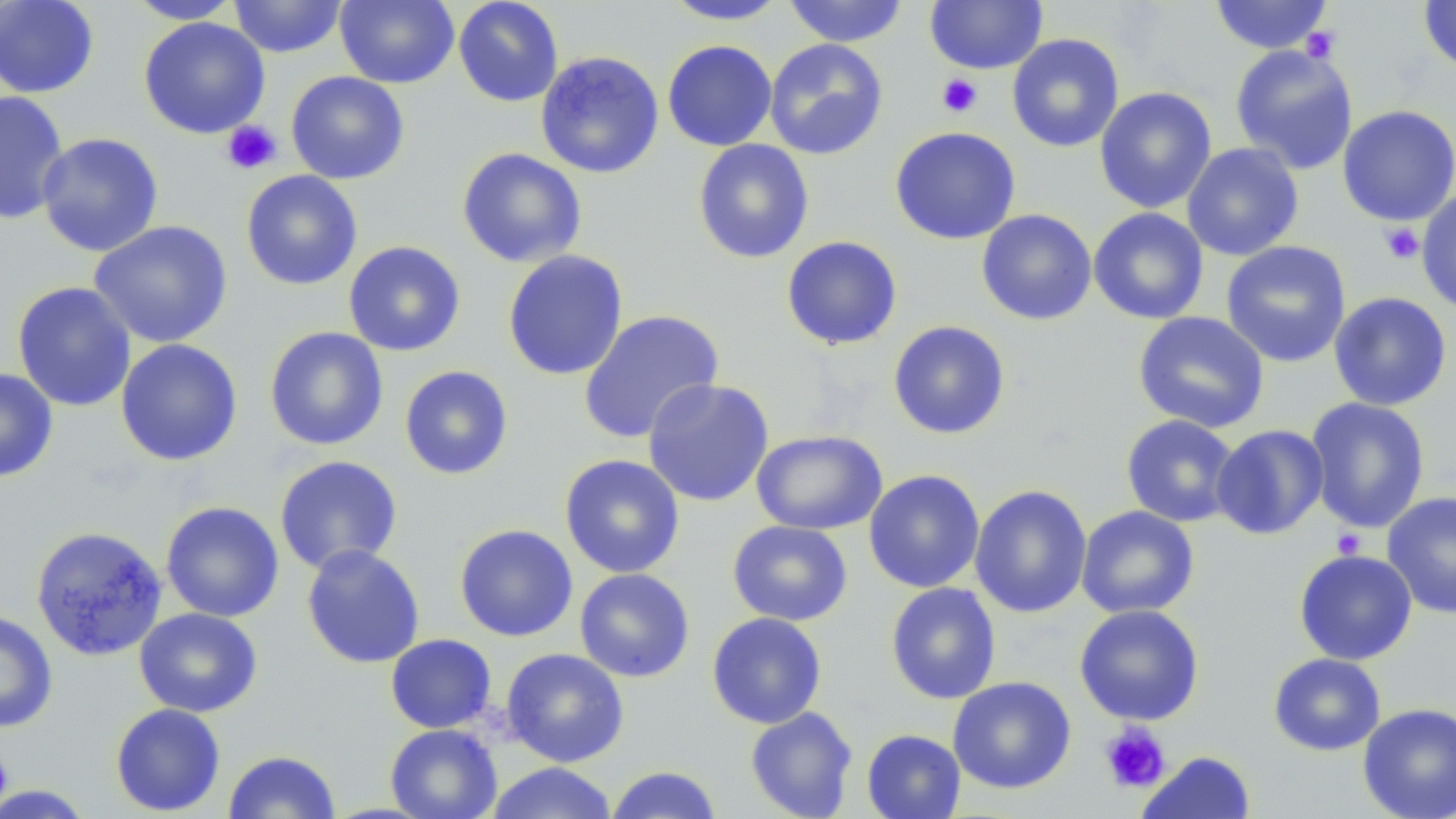
Summary:
  - Coordinate format: approximate bounding boxes as named x1/y1/x2/y2 corners in pixels
  - Platelet locations: (x1=1300, y1=26, x2=1341, y2=63), (x1=937, y1=73, x2=982, y2=118), (x1=221, y1=120, x2=283, y2=175), (x1=1379, y1=222, x2=1425, y2=265), (x1=1331, y1=528, x2=1366, y2=558), (x1=1099, y1=723, x2=1171, y2=793), (x1=0, y1=750, x2=13, y2=806)
  - Uninfected red blood cell locations: (x1=0, y1=0, x2=100, y2=98), (x1=126, y1=0, x2=244, y2=24), (x1=228, y1=0, x2=347, y2=58), (x1=335, y1=0, x2=459, y2=88), (x1=453, y1=0, x2=564, y2=107), (x1=783, y1=0, x2=910, y2=47), (x1=924, y1=0, x2=1048, y2=74), (x1=1209, y1=0, x2=1334, y2=55), (x1=662, y1=1, x2=790, y2=25), (x1=1418, y1=1, x2=1456, y2=74), (x1=138, y1=16, x2=270, y2=139), (x1=1007, y1=33, x2=1124, y2=152), (x1=764, y1=38, x2=888, y2=160), (x1=662, y1=40, x2=777, y2=152), (x1=1230, y1=44, x2=1358, y2=174), (x1=535, y1=51, x2=664, y2=179), (x1=286, y1=71, x2=410, y2=185), (x1=1095, y1=86, x2=1217, y2=214), (x1=1, y1=90, x2=70, y2=226), (x1=1337, y1=105, x2=1456, y2=226), (x1=889, y1=126, x2=1020, y2=245), (x1=37, y1=132, x2=164, y2=257), (x1=692, y1=139, x2=814, y2=264), (x1=1182, y1=142, x2=1304, y2=261), (x1=456, y1=148, x2=587, y2=268), (x1=240, y1=170, x2=363, y2=290), (x1=1416, y1=189, x2=1456, y2=315), (x1=1089, y1=207, x2=1209, y2=324), (x1=976, y1=209, x2=1097, y2=325), (x1=89, y1=220, x2=232, y2=348), (x1=780, y1=235, x2=903, y2=350), (x1=1221, y1=240, x2=1351, y2=367), (x1=343, y1=241, x2=465, y2=357), (x1=502, y1=250, x2=629, y2=381), (x1=12, y1=281, x2=137, y2=412), (x1=1329, y1=291, x2=1452, y2=411), (x1=578, y1=310, x2=724, y2=445), (x1=1133, y1=312, x2=1269, y2=433), (x1=887, y1=320, x2=1011, y2=440), (x1=264, y1=327, x2=388, y2=451), (x1=115, y1=339, x2=243, y2=466), (x1=399, y1=365, x2=513, y2=480), (x1=0, y1=368, x2=58, y2=482), (x1=642, y1=378, x2=774, y2=507), (x1=1305, y1=397, x2=1430, y2=533), (x1=1121, y1=415, x2=1241, y2=527), (x1=1211, y1=424, x2=1329, y2=540), (x1=751, y1=429, x2=887, y2=534), (x1=559, y1=454, x2=685, y2=578), (x1=274, y1=456, x2=403, y2=575), (x1=863, y1=469, x2=985, y2=593), (x1=970, y1=484, x2=1092, y2=618), (x1=1381, y1=491, x2=1456, y2=618), (x1=160, y1=501, x2=285, y2=622), (x1=1076, y1=505, x2=1200, y2=619), (x1=727, y1=520, x2=853, y2=626), (x1=454, y1=523, x2=578, y2=642), (x1=30, y1=526, x2=168, y2=662), (x1=301, y1=544, x2=425, y2=669), (x1=1293, y1=549, x2=1417, y2=665), (x1=574, y1=568, x2=695, y2=682), (x1=885, y1=582, x2=1001, y2=705), (x1=1074, y1=604, x2=1204, y2=725), (x1=134, y1=607, x2=263, y2=717), (x1=0, y1=610, x2=58, y2=733), (x1=706, y1=612, x2=827, y2=729), (x1=385, y1=633, x2=496, y2=733), (x1=501, y1=648, x2=629, y2=767), (x1=1268, y1=652, x2=1385, y2=756), (x1=947, y1=676, x2=1076, y2=794), (x1=1357, y1=702, x2=1456, y2=819), (x1=110, y1=703, x2=226, y2=816), (x1=745, y1=706, x2=858, y2=819), (x1=385, y1=724, x2=502, y2=819), (x1=1098, y1=728, x2=1174, y2=795), (x1=861, y1=729, x2=966, y2=819), (x1=223, y1=750, x2=341, y2=818), (x1=1137, y1=751, x2=1257, y2=818), (x1=484, y1=762, x2=619, y2=819), (x1=605, y1=765, x2=723, y2=819), (x1=0, y1=785, x2=95, y2=817)
  - Slide-level diagnosis: no evidence of blood parasites
  - Image size: 1456×819 pixels
  - Preparation: thin blood film
  - Field of view: one of a larger specimen
  - Stain: May-Grünwald-Giemsa
  - Modality: optical microscopy
  - Magnification: 1000x